Evaluate for parasitized red blood cells.
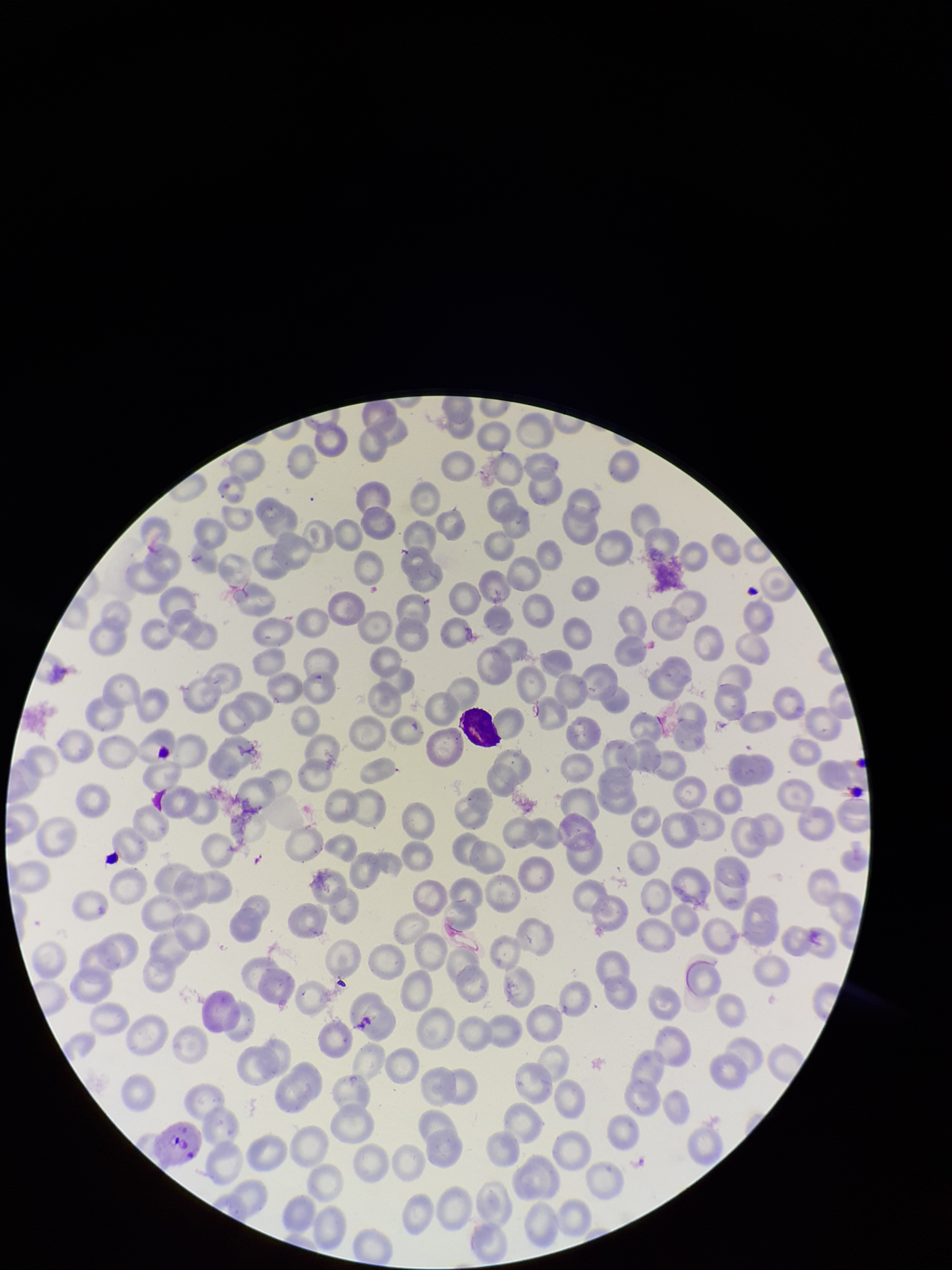

Identified.

Summary:
  - Parasitized red blood cell count: 1
  - Field of view: single
  - Species reported for this patient: Plasmodium vivax
  - Preparation: thin smear
  - Stain: Giemsa
  - Red blood cell count: 200
  - Capture: smartphone photograph through the microscope eyepiece
  - Patient malaria status: positive
  - Image size: 952×1270 pixels